Assess the morphology of the red blood cells.
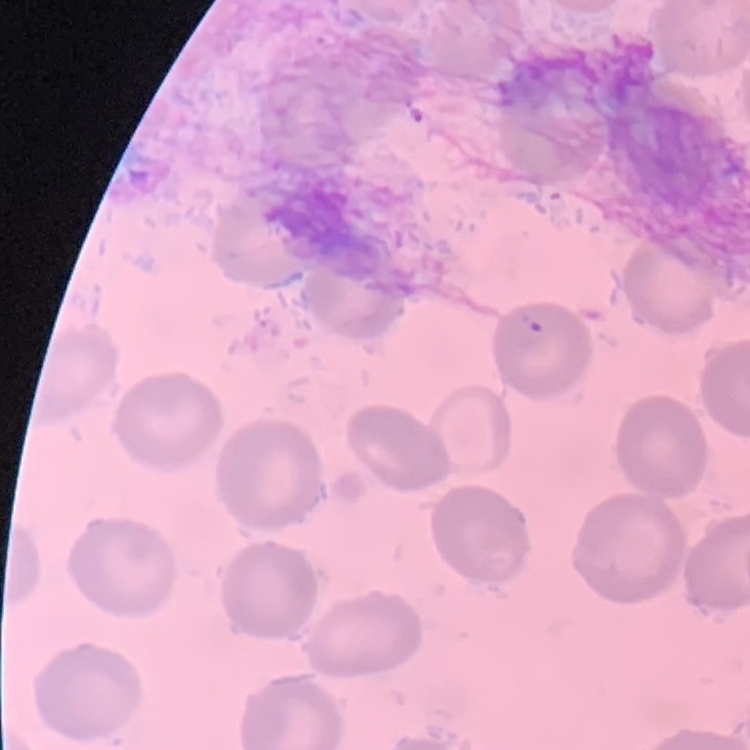

No rouleaux formation.

Summary:
  - Stain: Field's or Giemsa
  - Preparation: thin peripheral smear
  - Image type: square crop of a larger photomicrograph